Describe the morphology of the erythrocytes.
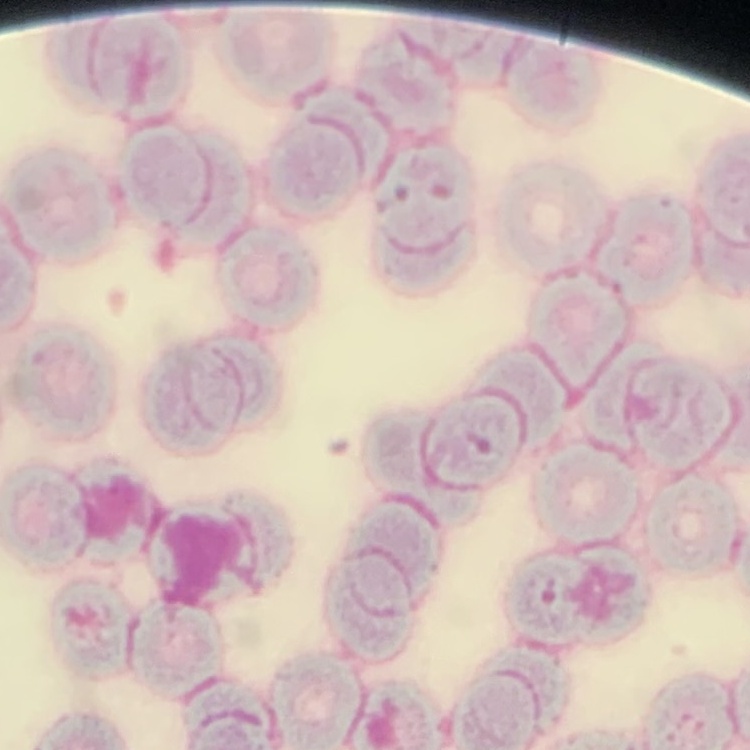

Rouleaux formation.

image type = one tile cut from a larger photomicrograph
stain = Field's or Giemsa
preparation = thin peripheral smear